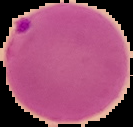
From a thin blood film. Segmented cell region on a black background. Image is 133×127 pixels. Malaria status: parasitized.